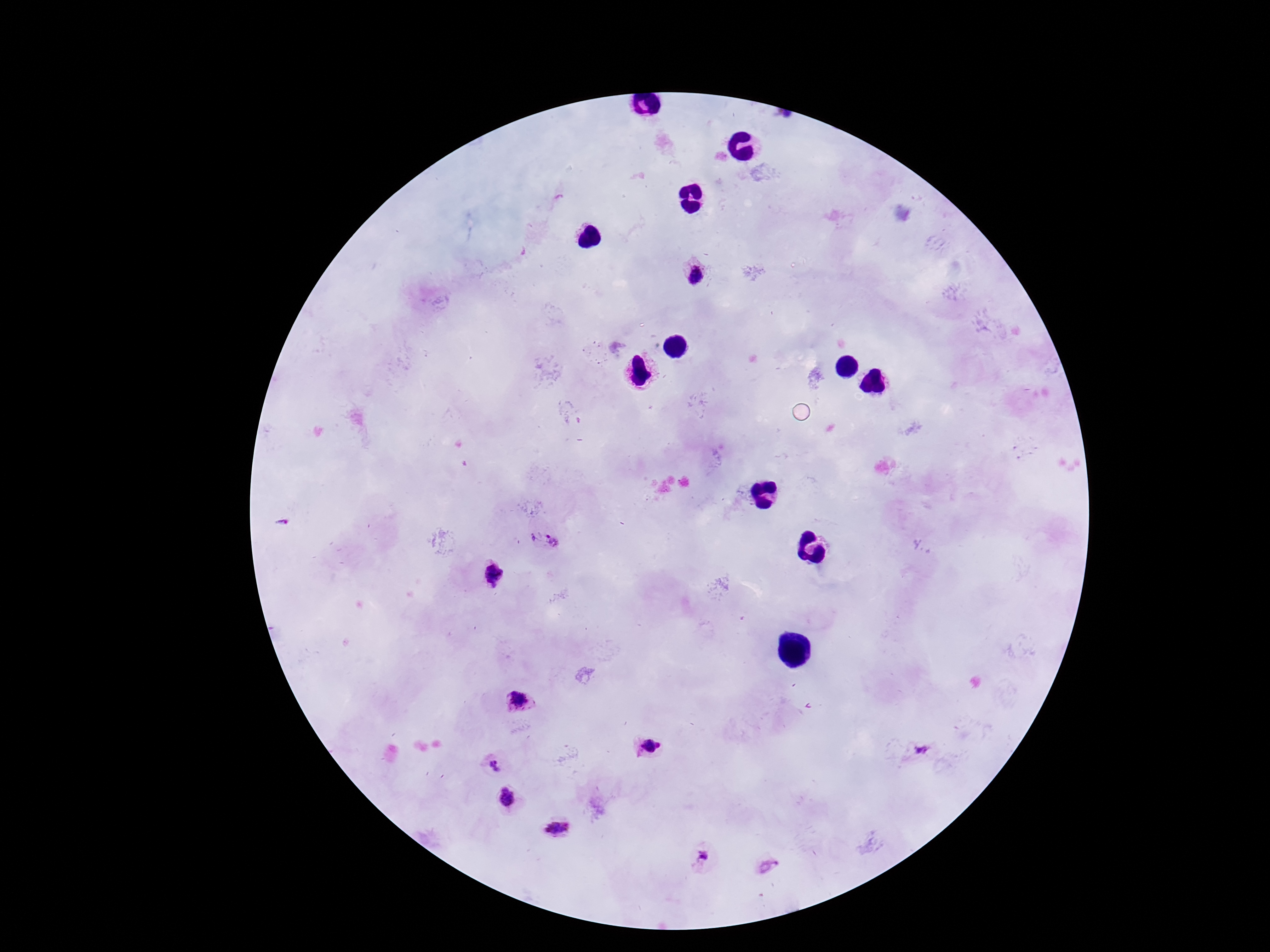

Approximate centers as [x, y] in pixels. Plasmodium parasite locations: [694, 275], [554, 541], [491, 575], [518, 700], [649, 745], [922, 749], [494, 766], [507, 797], [558, 828], [701, 855], [768, 866]. Thick blood film. Patient malaria status: positive. Giemsa-stained preparation. Photographed through the microscope eyepiece with a smartphone camera. Single field of view. 100x magnification. Image is 1270×952 pixels.